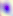

Captured at 400x magnification. Micrograph. Toxoplasma gondii is shown.